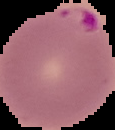

Result: Plasmodium parasites identified. Segmented cell region on a black background. Image is 115×130 pixels. From a thin blood smear.